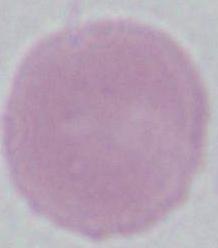

Summary:
  - Identification: red blood cell
  - Magnification: 1000x
  - Modality: micrograph